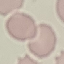
Result: negative for malaria parasites. Thin smear of blood. Automatically extracted cell patch, resized to 64 × 64 pixels. Photographed with a smartphone camera at the microscope eyepiece. Giemsa-stained preparation.